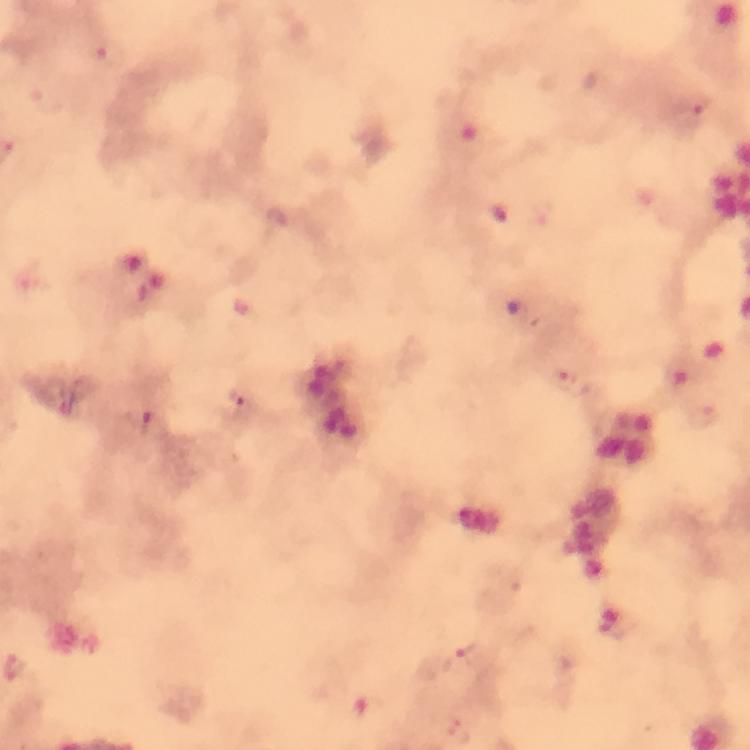 Approximate centers as (x, y) in pixels. Malaria parasite locations: (107, 53), (694, 103), (501, 214), (543, 214), (276, 219), (681, 373), (563, 380), (240, 397), (704, 416), (158, 425), (470, 655), (18, 669), (370, 710), (458, 732). Image is 750×750 pixels. From a malaria diagnostic workup. Giemsa-stained preparation. Immersion oil was used. At 100x magnification. A crop from one field of view. Thick blood smear. Smartphone photograph taken through a microscope.